Identify the parasite.
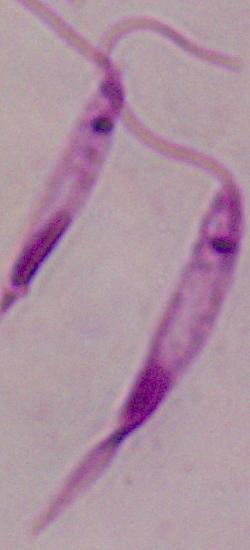
Leishmania.

Summary:
  - Modality: micrograph
  - Magnification: 1000x